Report the malaria status of this cell.
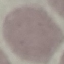
Uninfected.

Acquired by smartphone through the microscope eyepiece. Thin blood film. Automatically extracted cell patch, resized to 64 × 64 pixels. Giemsa stain.